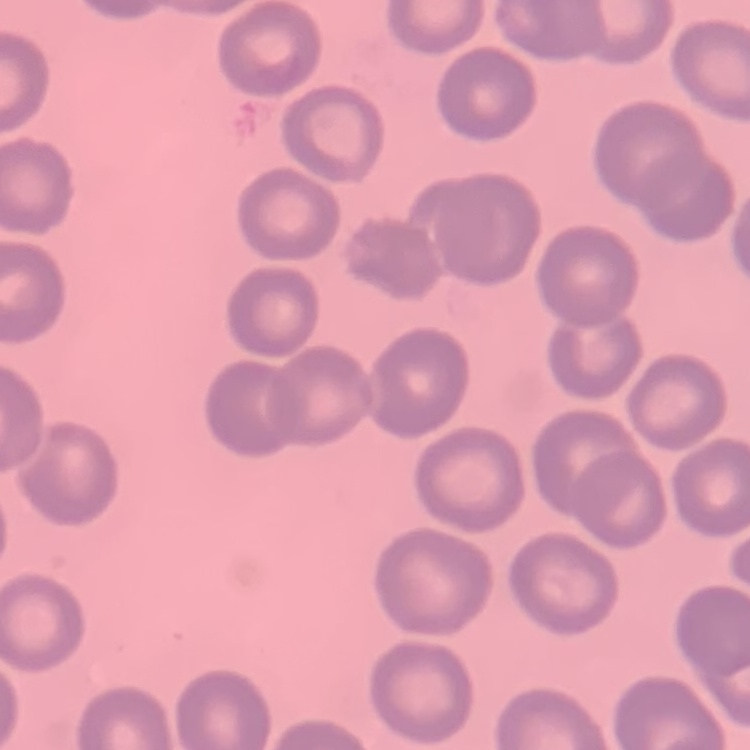

The erythrocytes show no rouleaux formation. Square crop of a larger photomicrograph. Thin peripheral smear. Stained with either Field's or Giemsa.